Give the extent of all Plasmodium ovale-infected red blood cells.
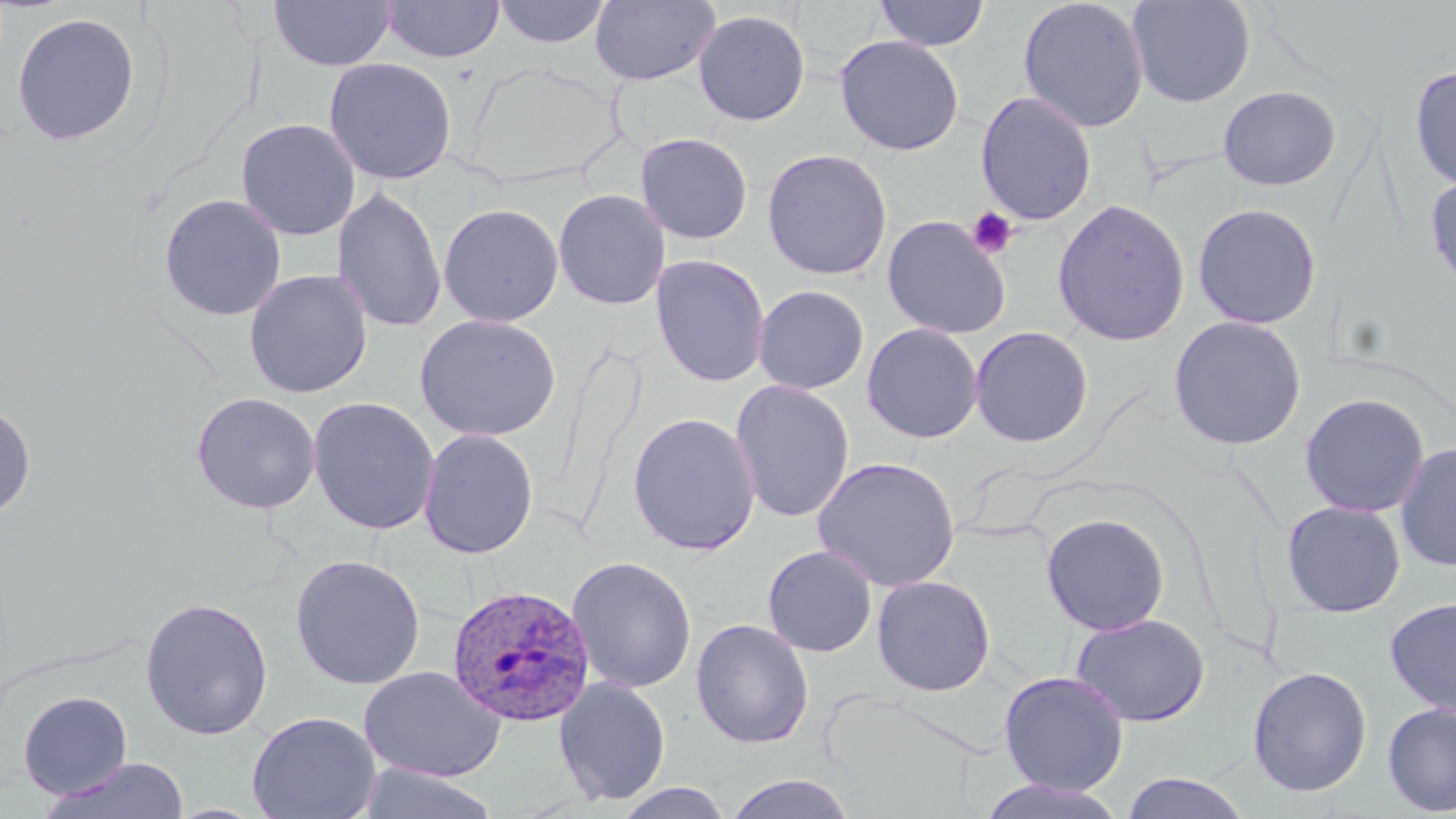
Approximate bounding boxes as [x1, y1, x2, y2] in pixels.
Plasmodium ovale-infected red blood cells: [446, 583, 596, 726].

{
  "slide_level_diagnosis": "Plasmodium ovale",
  "uninfected_red_blood_cell_locations": "approximate bounding boxes as [x1, y1, x2, y2] in pixels: [269, 0, 396, 71], [381, 0, 505, 63], [493, 0, 612, 48], [590, 0, 721, 86], [873, 0, 990, 52], [1017, 0, 1150, 133], [1126, 0, 1256, 108], [693, 8, 811, 126], [10, 11, 142, 147], [834, 35, 965, 156], [323, 57, 458, 184], [1408, 64, 1456, 192], [1217, 85, 1342, 191], [975, 91, 1097, 226], [235, 118, 361, 241], [635, 132, 754, 245], [761, 148, 893, 280], [1424, 170, 1456, 296], [332, 186, 447, 334], [553, 188, 670, 310], [158, 193, 287, 322], [1052, 197, 1190, 347], [1192, 202, 1322, 330], [438, 203, 564, 327], [881, 215, 1012, 340], [650, 254, 771, 388], [243, 269, 373, 398], [752, 285, 869, 394], [414, 314, 562, 441], [1167, 315, 1307, 451], [862, 323, 983, 444], [969, 325, 1094, 448], [730, 379, 855, 523], [190, 391, 321, 514], [1299, 392, 1430, 517], [307, 396, 440, 535], [0, 400, 36, 521], [626, 412, 762, 557], [418, 427, 539, 560], [1394, 441, 1456, 572], [812, 456, 962, 592], [1281, 500, 1406, 617], [1040, 513, 1170, 636], [762, 545, 878, 657], [289, 554, 426, 690], [566, 555, 697, 693], [872, 574, 996, 697], [139, 595, 274, 740], [1384, 597, 1456, 718], [1070, 613, 1211, 727], [691, 618, 814, 749], [358, 665, 507, 783], [1247, 665, 1373, 798], [998, 671, 1129, 796], [553, 676, 671, 807], [17, 690, 133, 799], [1382, 702, 1456, 816], [247, 711, 381, 819], [37, 756, 191, 818], [352, 763, 502, 819], [1120, 772, 1252, 818], [722, 774, 858, 818], [975, 778, 1130, 818], [612, 782, 735, 819]",
  "preparation": "thin blood film",
  "field_of_view": "one of a larger specimen",
  "stain": "May-Grünwald-Giemsa",
  "magnification": "1000x",
  "platelet_locations": "approximate bounding boxes as [x1, y1, x2, y2] in pixels: [966, 205, 1019, 260]",
  "image_size": "1456×819 pixels",
  "modality": "light microscopy"
}